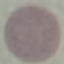
Summary:
  - Malaria status: uninfected
  - Image type: cell patch, automatically extracted from a larger field of view and resized to 64 × 64 pixels
  - Preparation: thin blood smear
  - Capture: smartphone through the microscope eyepiece
  - Stain: Giemsa